Give the extent of all Plasmodium falciparum-infected red blood cells.
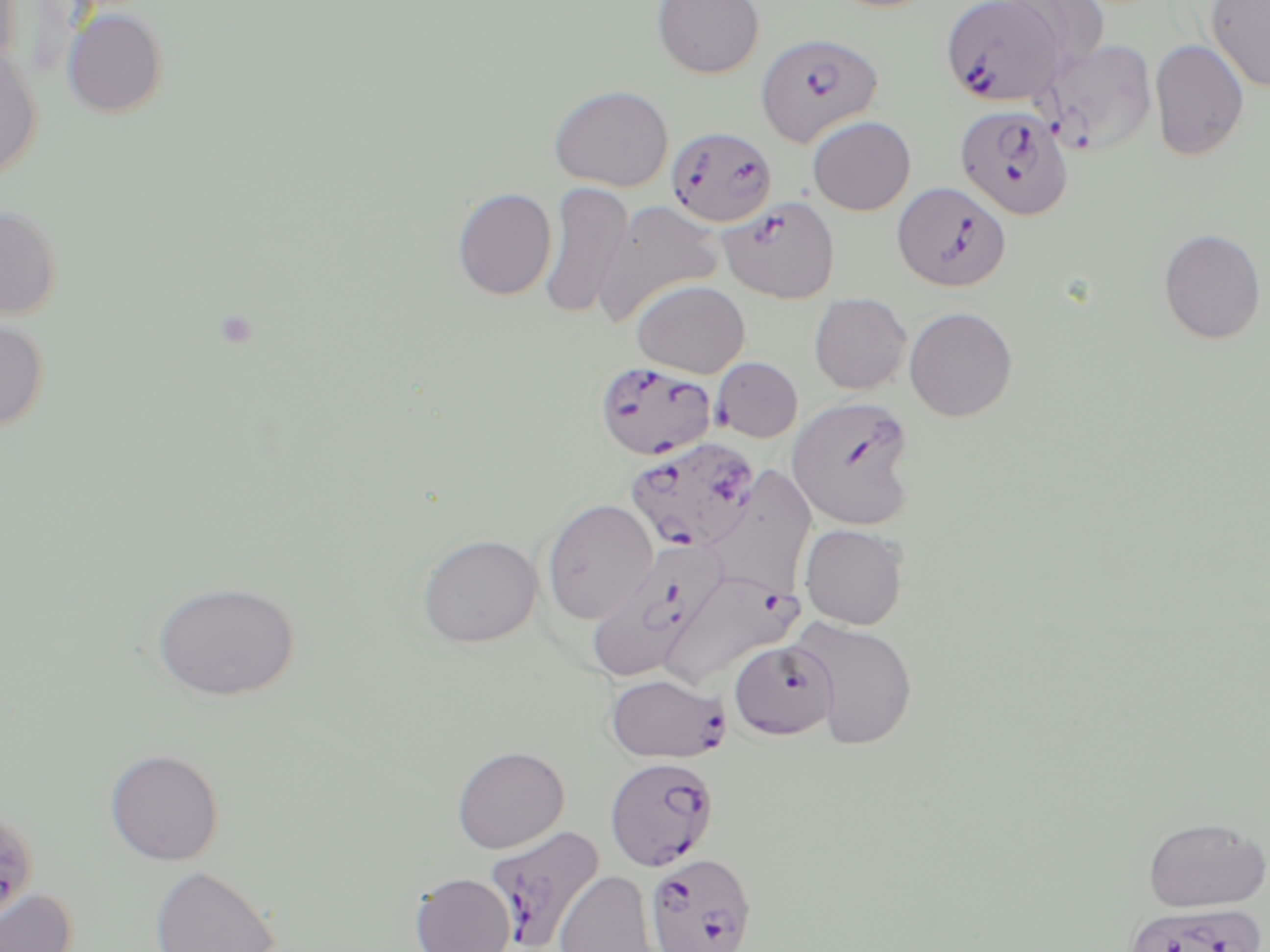

Approximate bounding boxes as [x1, y1, x2, y2] in pixels.
Plasmodium falciparum-infected red blood cells: [940, 0, 1065, 106], [755, 32, 883, 147], [954, 104, 1074, 221], [666, 126, 778, 228], [892, 181, 1011, 292], [717, 195, 840, 304], [711, 357, 803, 442], [594, 359, 717, 460], [786, 395, 918, 530], [625, 437, 764, 555], [587, 537, 726, 682], [659, 569, 799, 692], [728, 640, 840, 740], [604, 672, 730, 763], [605, 757, 718, 871], [1, 808, 40, 926], [484, 826, 605, 951], [646, 852, 758, 952].

Summary:
  - Uninfected red blood cell locations: [12, 0, 91, 85], [652, 0, 765, 78], [997, 0, 1110, 76], [1206, 1, 1270, 93], [62, 7, 169, 119], [1039, 38, 1158, 157], [1149, 39, 1250, 161], [0, 43, 42, 181], [548, 84, 674, 192], [807, 115, 916, 216], [538, 181, 633, 320], [452, 187, 557, 300], [593, 199, 724, 327], [0, 203, 64, 320], [1158, 227, 1267, 344], [632, 279, 750, 378], [809, 292, 912, 395], [904, 306, 1018, 422], [0, 316, 50, 433], [704, 465, 817, 601], [541, 498, 659, 625], [800, 523, 909, 629], [416, 533, 542, 647], [150, 580, 301, 702], [790, 616, 919, 750], [451, 745, 570, 853], [104, 748, 224, 866], [1142, 816, 1269, 912], [150, 864, 280, 952], [554, 870, 659, 952], [410, 873, 515, 952], [0, 886, 76, 951]
  - Slide-level diagnosis: Plasmodium falciparum
  - Field of view: one of a larger specimen
  - Magnification: 1000x
  - Image size: 1270×952 pixels
  - Preparation: thin blood film
  - Stain: May-Grünwald-Giemsa
  - Modality: optical microscopy